Assess the morphology of the red blood cells.
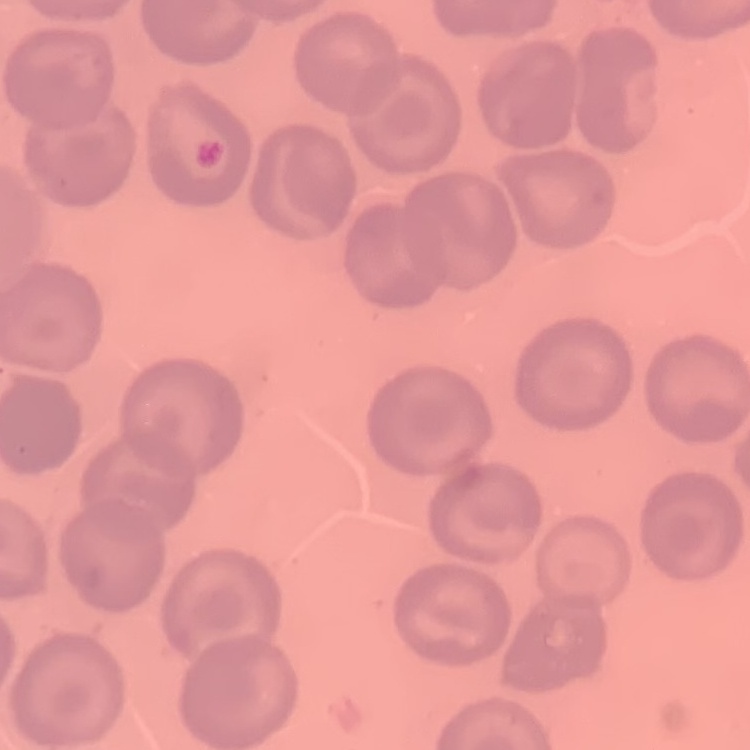
They show no rouleaux formation.

preparation = thin blood film
stain = Field's or Giemsa
image type = square crop of a larger photomicrograph